Identify the parasite.
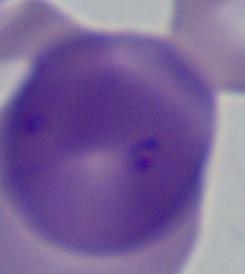

Babesia.

Summary:
  - Modality: micrograph
  - Magnification: 1000x